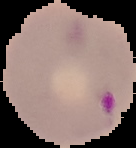

Summary:
  - Image type: segmented cell region with the area outside set to black
  - Image size: 136×148 pixels
  - Result: Plasmodium parasites identified
  - Preparation: thin blood film